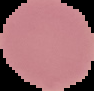

image size = 94×91 pixels
image type = cell region segmented out of the field of view; surrounding area masked to black
preparation = thin blood film
result = no Plasmodium parasites detected